Assess this cell for malaria.
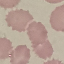

Uninfected.

stain = Giemsa
capture = smartphone camera at the microscope eyepiece
image type = automatically extracted cell patch, resized to 64 × 64 pixels
preparation = thin blood film